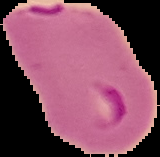
Summary:
  - Image type: segmented cell region on a black background
  - Result: malaria parasites detected
  - Preparation: thin blood smear
  - Image size: 160×157 pixels